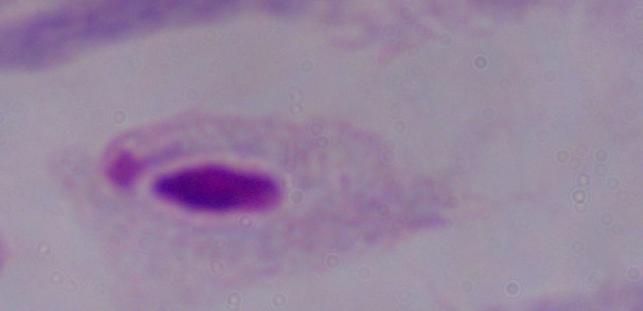
modality = photomicrograph
identification = trichomonad
magnification = 1000x